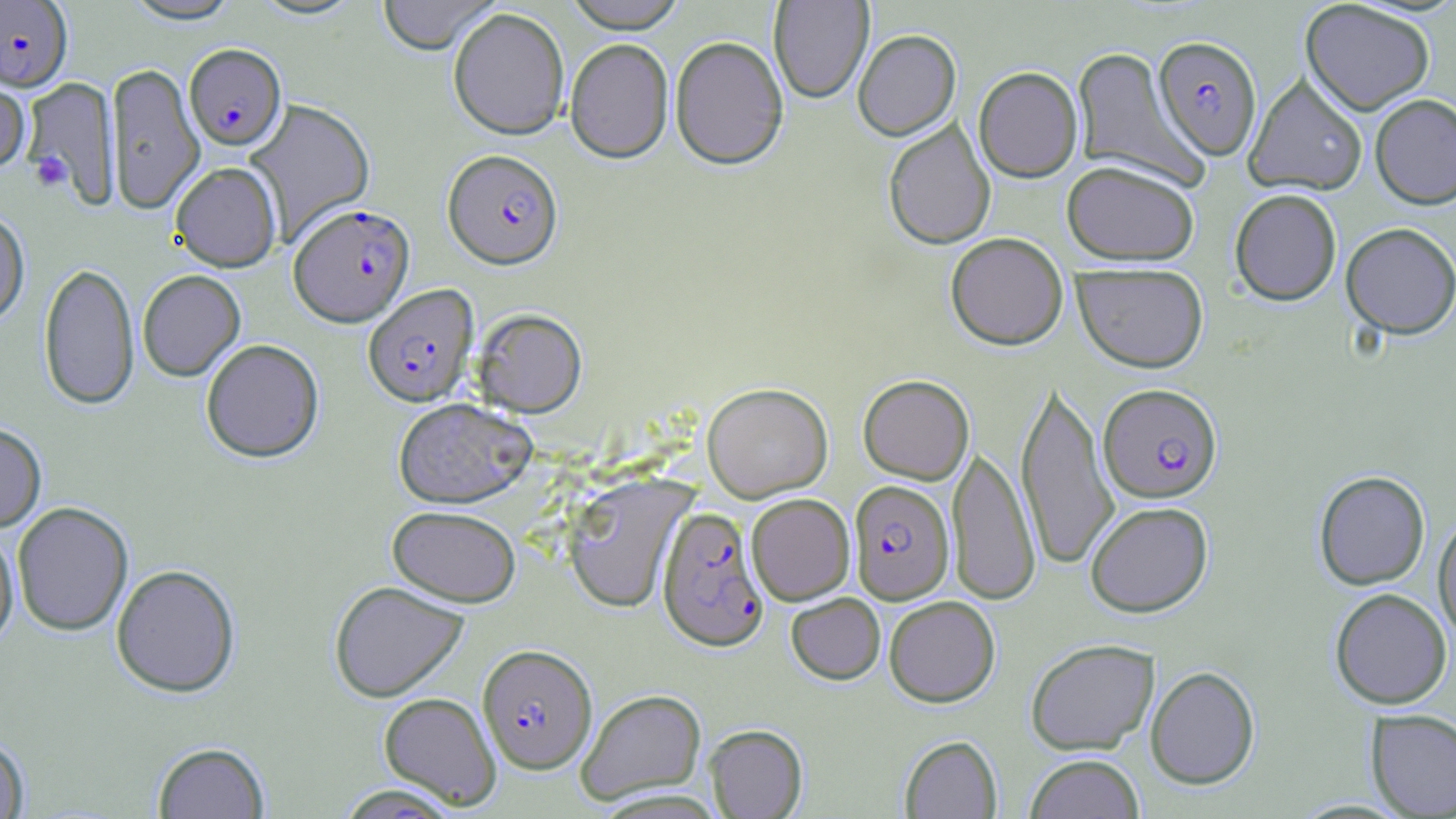
{
  "plasmodium_falciparum_infected_red_blood_cell_locations": "approximate bounding boxes as [x1, y1, x2, y2] in pixels: [0, 0, 73, 93], [1153, 36, 1262, 159], [184, 45, 286, 152], [443, 150, 563, 270], [289, 204, 415, 326], [362, 284, 480, 408], [1099, 383, 1222, 502], [848, 480, 954, 605], [657, 507, 769, 652], [477, 644, 597, 774]",
  "slide_level_diagnosis": "Plasmodium falciparum",
  "modality": "optical microscopy",
  "field_of_view": "single",
  "preparation": "thin blood smear",
  "stain": "May-Grünwald-Giemsa",
  "platelet_locations": "approximate bounding boxes as [x1, y1, x2, y2] in pixels: [29, 152, 71, 192]",
  "magnification": "1000x",
  "uninfected_red_blood_cell_locations": "approximate bounding boxes as [x1, y1, x2, y2] in pixels: [121, 0, 243, 25], [250, 0, 367, 22], [377, 0, 501, 57], [563, 0, 688, 34], [769, 0, 874, 104], [1300, 1, 1435, 115], [448, 9, 569, 142], [853, 29, 961, 141], [670, 36, 789, 171], [565, 39, 673, 164], [1072, 46, 1205, 189], [106, 63, 204, 213], [973, 66, 1082, 182], [1244, 74, 1368, 196], [0, 76, 30, 177], [23, 77, 120, 207], [1370, 93, 1456, 210], [245, 98, 375, 244], [883, 119, 996, 250], [1061, 160, 1200, 266], [170, 162, 282, 272], [1229, 188, 1342, 305], [0, 211, 30, 328], [1341, 222, 1456, 339], [945, 232, 1068, 350], [38, 261, 139, 411], [1072, 262, 1209, 372], [137, 270, 245, 382], [472, 308, 587, 417], [201, 339, 324, 463], [858, 374, 974, 484], [1016, 376, 1119, 572], [702, 382, 833, 501], [392, 397, 537, 509], [0, 422, 47, 532], [948, 443, 1041, 606], [1313, 470, 1430, 590], [563, 474, 696, 614], [746, 493, 855, 605], [1085, 501, 1213, 617], [12, 502, 133, 637], [387, 505, 520, 607], [1433, 511, 1456, 644], [0, 527, 19, 650], [111, 564, 241, 698], [328, 580, 468, 702], [1330, 588, 1452, 709], [786, 593, 885, 684], [884, 596, 1000, 707], [1025, 638, 1159, 755], [1145, 665, 1260, 789], [576, 688, 706, 804], [378, 692, 501, 808], [1366, 709, 1456, 817], [704, 724, 808, 818], [0, 735, 30, 819], [899, 735, 1002, 818], [152, 741, 271, 818], [1025, 754, 1145, 819], [333, 784, 464, 818]",
  "image_size": "1456×819 pixels"
}